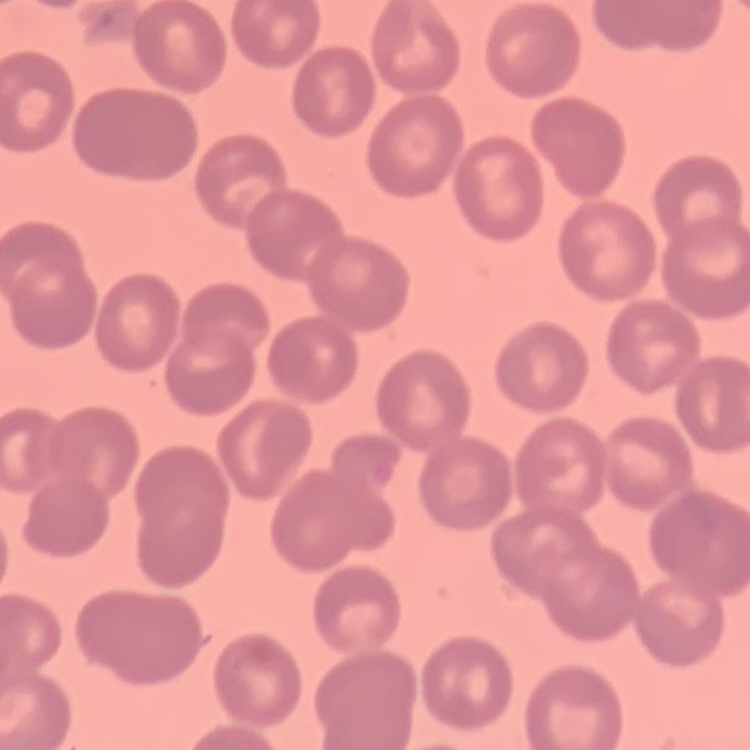

The erythrocytes show no rouleaux formation. Thin blood smear. One tile cut from a larger photomicrograph. Stained with either Field's or Giemsa.